Name the blood parasite species.
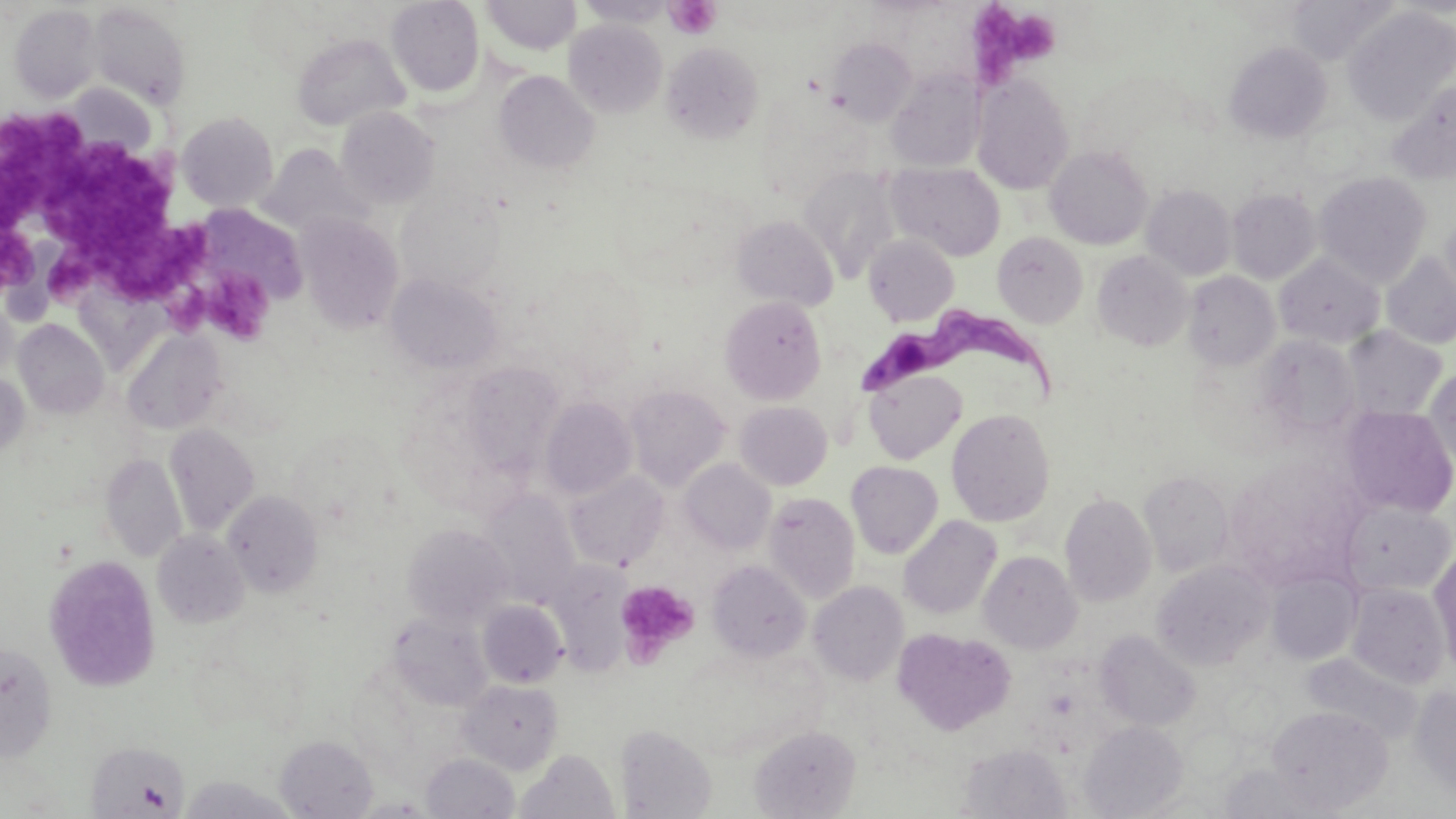

Trypanosoma brucei.

{
  "preparation": "thin blood film",
  "modality": "optical microscopy",
  "field_of_view": "one of a larger specimen",
  "platelet_locations": "approximate bounding boxes as [x1, y1, x2, y2] in pixels: [665, 1, 720, 39], [969, 2, 1056, 82], [0, 113, 99, 229], [43, 145, 181, 250], [0, 227, 40, 292], [52, 228, 214, 308], [201, 266, 275, 344], [615, 579, 701, 663]",
  "magnification": "1000x",
  "trypanosoma_brucei_locations": "approximate bounding boxes as [x1, y1, x2, y2] in pixels: [849, 301, 1060, 408]",
  "stain": "May-Grünwald-Giemsa",
  "uninfected_red_blood_cell_locations": "approximate bounding boxes as [x1, y1, x2, y2] in pixels: [481, 0, 581, 56], [576, 0, 676, 27], [386, 1, 485, 97], [87, 3, 191, 109], [9, 4, 101, 103], [1343, 6, 1456, 126], [564, 20, 666, 117], [292, 33, 410, 132], [827, 37, 916, 125], [1224, 41, 1332, 143], [662, 42, 763, 142], [493, 70, 599, 174], [886, 70, 985, 172], [972, 73, 1074, 195], [1388, 80, 1456, 184], [336, 107, 440, 208], [177, 111, 279, 212], [257, 145, 371, 239], [1045, 145, 1153, 250], [887, 162, 1005, 261], [799, 166, 899, 281], [1315, 171, 1431, 286], [1141, 184, 1236, 280], [1227, 188, 1321, 284], [1440, 213, 1456, 306], [297, 214, 404, 334], [731, 215, 838, 310], [992, 232, 1088, 328], [863, 234, 959, 326], [1092, 250, 1193, 351], [1381, 252, 1456, 350], [1275, 253, 1384, 348], [1183, 271, 1281, 371], [386, 272, 503, 375], [719, 295, 826, 404], [13, 318, 109, 419], [1342, 326, 1447, 420], [121, 328, 227, 435], [1259, 334, 1362, 436], [458, 361, 566, 478], [1424, 367, 1456, 471], [863, 368, 968, 465], [1, 372, 29, 458], [625, 384, 731, 491], [539, 397, 637, 501], [734, 401, 833, 490], [1340, 407, 1456, 519], [946, 408, 1055, 526], [164, 424, 259, 536], [101, 453, 186, 562], [678, 458, 776, 555], [846, 461, 943, 559], [1226, 464, 1348, 582], [1139, 470, 1235, 577], [565, 471, 669, 570], [478, 489, 581, 605], [223, 490, 323, 597], [763, 492, 859, 604], [1059, 492, 1156, 607], [1339, 500, 1454, 596], [898, 515, 1002, 620], [402, 523, 513, 627], [152, 530, 250, 628], [1430, 548, 1456, 677], [978, 550, 1082, 653], [44, 555, 162, 691], [707, 559, 811, 662], [1151, 559, 1274, 670], [548, 566, 632, 675], [1266, 568, 1362, 664], [808, 580, 908, 686], [1348, 583, 1449, 688], [478, 600, 568, 688], [389, 611, 494, 711], [893, 628, 1016, 736], [1095, 630, 1201, 731], [0, 641, 56, 761], [1303, 653, 1424, 747], [457, 678, 564, 773], [1409, 685, 1456, 794], [1267, 705, 1393, 813], [1079, 721, 1187, 818], [615, 724, 716, 818], [748, 725, 861, 818], [275, 735, 378, 818], [86, 740, 190, 816], [958, 743, 1073, 818], [517, 749, 618, 819], [421, 752, 519, 818], [178, 774, 300, 818]",
  "image_size": "1456×819 pixels"
}